Locate every Plasmodium parasite.
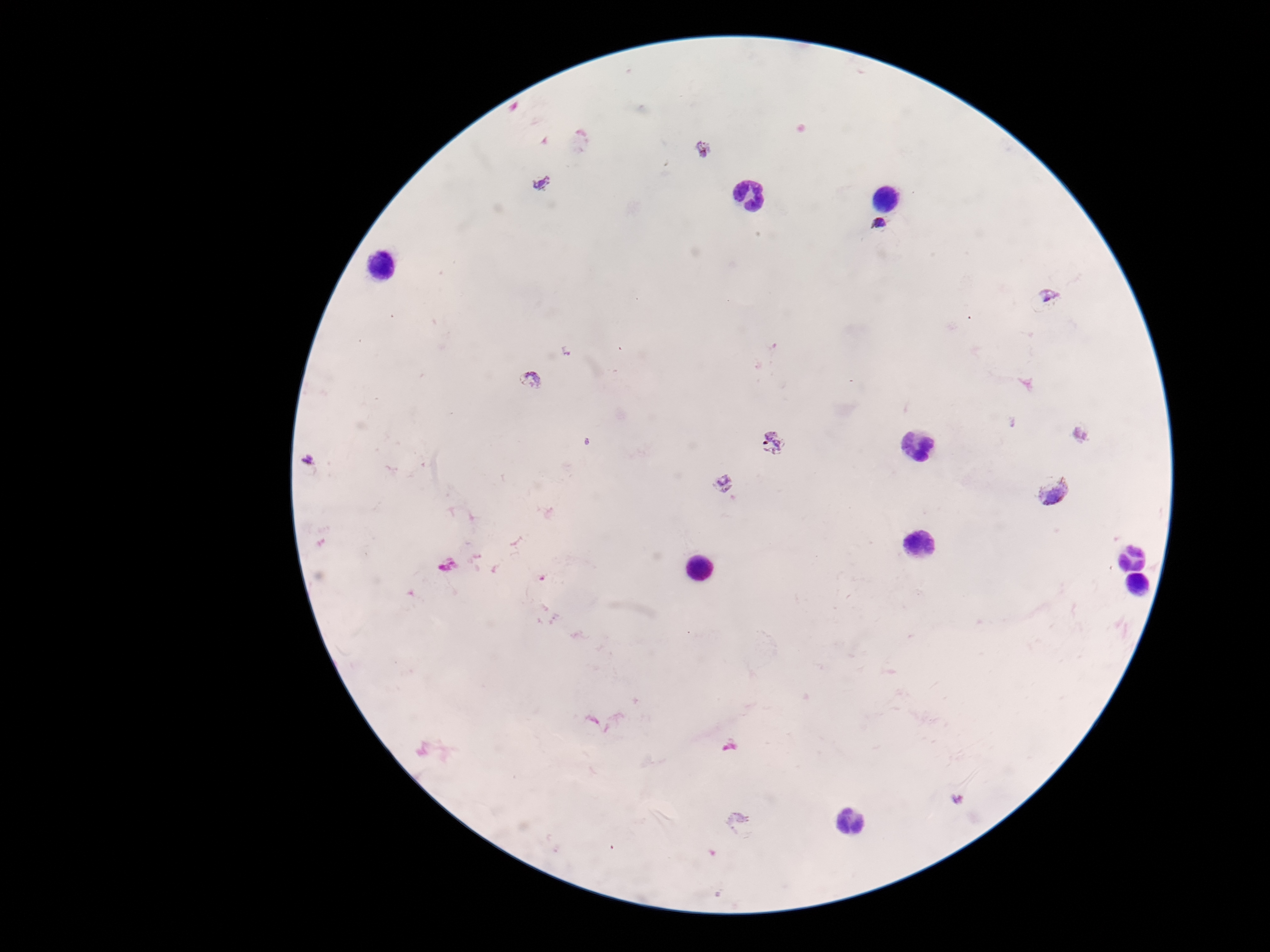

Approximate centers as {x, y} in pixels.
Plasmodium parasites: {703, 148}, {541, 182}, {880, 224}, {1049, 296}, {567, 350}, {531, 378}, {1080, 434}, {773, 442}, {307, 458}, {722, 483}, {1054, 490}, {958, 799}.

Summary:
  - Patient malaria status: positive
  - Preparation: thick peripheral-blood smear
  - Capture: smartphone camera through the microscope eyepiece
  - Field of view: one from this slide
  - Magnification: 100x
  - Stain: Giemsa
  - Image size: 1270×952 pixels